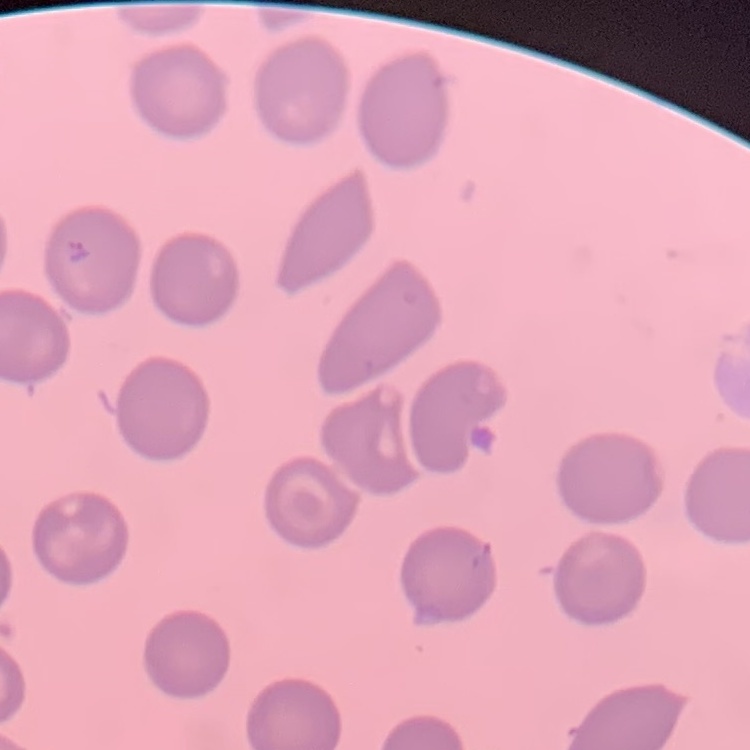

Summary:
  - Red blood cell morphology: no rouleaux formation
  - Stain: Field's or Giemsa
  - Image type: one tile cut from a larger photomicrograph
  - Preparation: thin blood smear